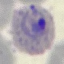
Malaria status: parasitized. Cell patch, automatically extracted from a larger field of view and resized to 64 × 64 pixels. Photographed with a smartphone camera at the microscope eyepiece. Giemsa-stained preparation. Thin blood film.